Outline each blood parasite and name the species.
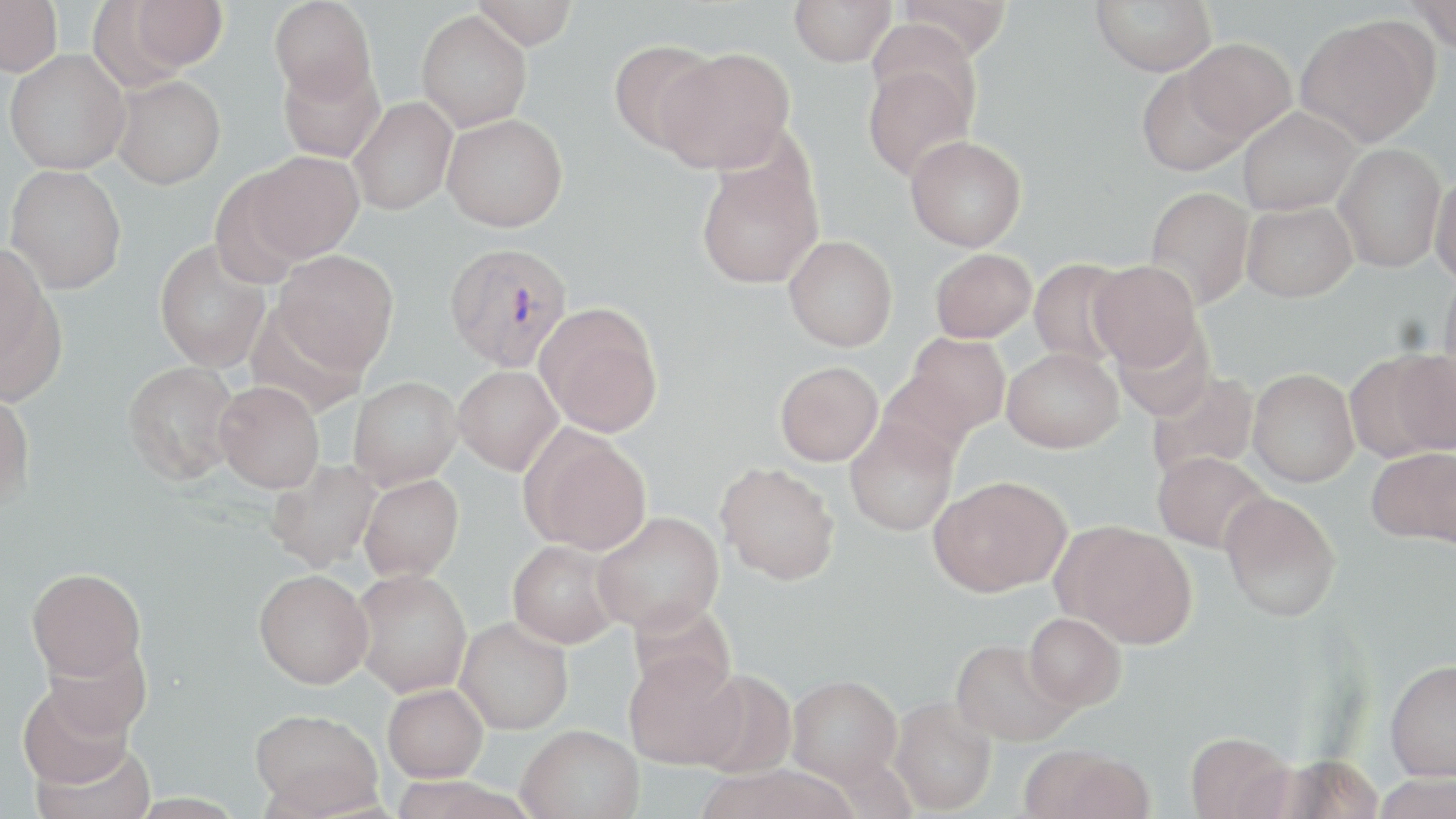
Approximate bounding boxes as named x1/y1/x2/y2 corners in pixels.
Plasmodium vivax-infected red blood cells: (x1=444, y1=241, x2=574, y2=372).
No Plasmodium falciparum, Plasmodium ovale, Plasmodium malariae, Babesia divergens, or Trypanosoma brucei observed.

Summary:
  - Uninfected red blood cell locations: (x1=0, y1=0, x2=62, y2=77), (x1=269, y1=0, x2=377, y2=104), (x1=472, y1=0, x2=578, y2=49), (x1=789, y1=0, x2=897, y2=66), (x1=895, y1=0, x2=1012, y2=59), (x1=1091, y1=0, x2=1216, y2=75), (x1=1407, y1=0, x2=1456, y2=53), (x1=120, y1=1, x2=228, y2=75), (x1=416, y1=10, x2=532, y2=132), (x1=1295, y1=17, x2=1436, y2=146), (x1=1183, y1=38, x2=1297, y2=142), (x1=608, y1=40, x2=720, y2=154), (x1=658, y1=47, x2=795, y2=173), (x1=4, y1=50, x2=129, y2=174), (x1=861, y1=59, x2=979, y2=181), (x1=278, y1=60, x2=385, y2=164), (x1=1136, y1=65, x2=1252, y2=176), (x1=112, y1=75, x2=226, y2=189), (x1=348, y1=97, x2=457, y2=216), (x1=1236, y1=107, x2=1361, y2=215), (x1=442, y1=114, x2=567, y2=232), (x1=905, y1=135, x2=1026, y2=251), (x1=1333, y1=144, x2=1446, y2=272), (x1=247, y1=151, x2=364, y2=263), (x1=696, y1=157, x2=823, y2=289), (x1=5, y1=165, x2=127, y2=294), (x1=209, y1=172, x2=311, y2=287), (x1=1429, y1=173, x2=1456, y2=286), (x1=1145, y1=187, x2=1256, y2=310), (x1=1241, y1=202, x2=1357, y2=302), (x1=784, y1=235, x2=897, y2=351), (x1=154, y1=239, x2=271, y2=373), (x1=0, y1=244, x2=59, y2=387), (x1=930, y1=248, x2=1036, y2=343), (x1=271, y1=249, x2=400, y2=375), (x1=1029, y1=258, x2=1132, y2=367), (x1=1088, y1=260, x2=1202, y2=371), (x1=1439, y1=266, x2=1456, y2=394), (x1=536, y1=304, x2=663, y2=437), (x1=1111, y1=318, x2=1216, y2=420), (x1=902, y1=333, x2=1010, y2=438), (x1=1002, y1=348, x2=1123, y2=452), (x1=1380, y1=350, x2=1456, y2=458), (x1=122, y1=361, x2=241, y2=485), (x1=775, y1=361, x2=883, y2=466), (x1=453, y1=365, x2=563, y2=475), (x1=1248, y1=368, x2=1359, y2=487), (x1=876, y1=369, x2=978, y2=471), (x1=1146, y1=372, x2=1260, y2=482), (x1=348, y1=377, x2=462, y2=489), (x1=214, y1=381, x2=325, y2=493), (x1=0, y1=387, x2=35, y2=511), (x1=845, y1=419, x2=959, y2=536), (x1=520, y1=427, x2=652, y2=554), (x1=1368, y1=447, x2=1456, y2=545), (x1=1153, y1=451, x2=1272, y2=554), (x1=265, y1=458, x2=382, y2=572), (x1=716, y1=462, x2=840, y2=584), (x1=359, y1=474, x2=463, y2=582), (x1=929, y1=476, x2=1071, y2=596), (x1=1220, y1=491, x2=1342, y2=622), (x1=592, y1=511, x2=724, y2=635), (x1=1055, y1=521, x2=1197, y2=647), (x1=508, y1=540, x2=622, y2=648), (x1=26, y1=567, x2=147, y2=683), (x1=254, y1=569, x2=373, y2=688), (x1=351, y1=569, x2=473, y2=697), (x1=1024, y1=613, x2=1126, y2=710), (x1=455, y1=617, x2=573, y2=734), (x1=38, y1=635, x2=151, y2=741), (x1=950, y1=638, x2=1077, y2=747), (x1=623, y1=650, x2=744, y2=769), (x1=1384, y1=659, x2=1456, y2=781), (x1=689, y1=669, x2=796, y2=778), (x1=786, y1=674, x2=902, y2=785), (x1=17, y1=677, x2=139, y2=791), (x1=383, y1=683, x2=487, y2=782), (x1=889, y1=696, x2=996, y2=815), (x1=249, y1=708, x2=383, y2=815), (x1=517, y1=724, x2=643, y2=819), (x1=1185, y1=732, x2=1296, y2=819), (x1=1018, y1=745, x2=1152, y2=819), (x1=1372, y1=773, x2=1456, y2=819)
  - Slide-level diagnosis: Plasmodium vivax
  - Image size: 1456×819 pixels
  - Modality: optical microscopy
  - Preparation: thin blood film
  - Magnification: 1000x
  - Field of view: one of a larger specimen
  - Stain: May-Grünwald-Giemsa